Give the preparation type.
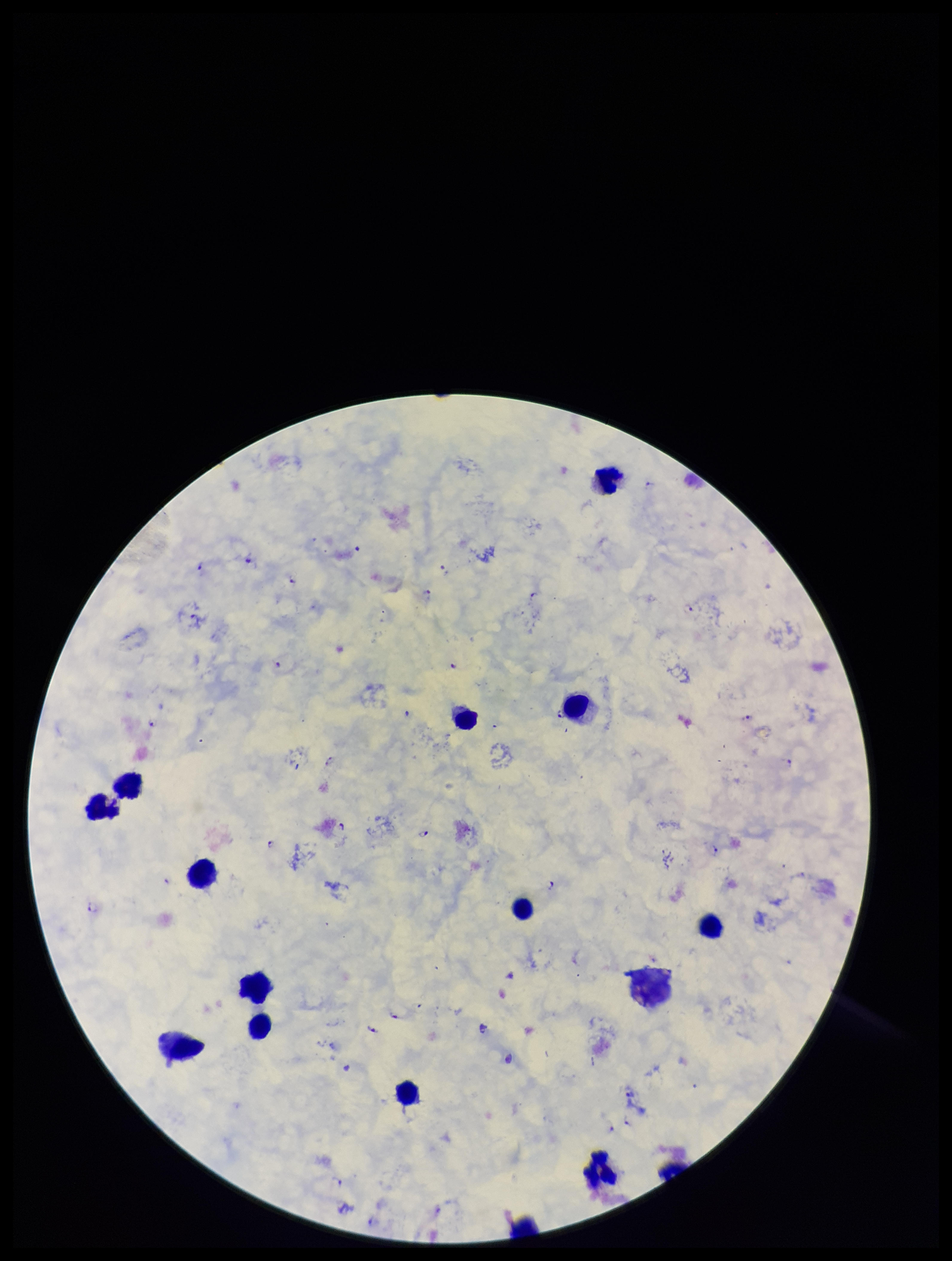

A thick smear.

Species reported for this patient: Plasmodium falciparum. Plasmodium parasites: detected. Photographed through the microscope eyepiece with a smartphone camera. Leukocyte count: 16. Parasite count: 42. Image is 952×1261 pixels. Patient malaria status: infected. Giemsa stain. One field from this slide.